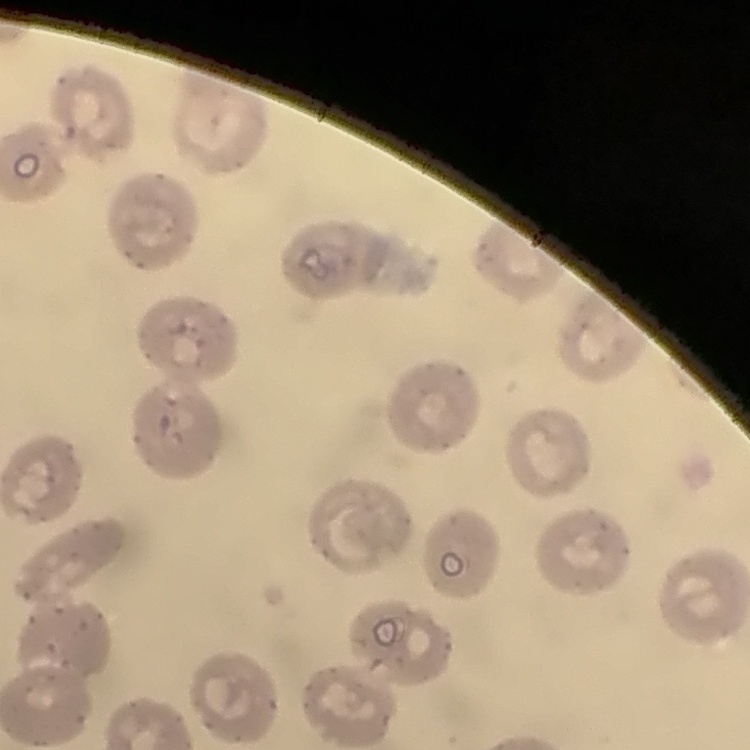

red blood cell morphology = no rouleaux formation
preparation = thin peripheral smear
image type = one tile cut from a larger photomicrograph
stain = Field's or Giemsa